Name the parasite shown.
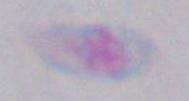
This is Toxoplasma gondii.

Captured at 1000x magnification. Photomicrograph.